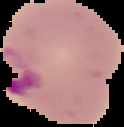
{
  "malaria_status": "parasitized",
  "image_size": "124×127 pixels",
  "preparation": "thin blood smear",
  "image_type": "segmented cell region on a black background"
}